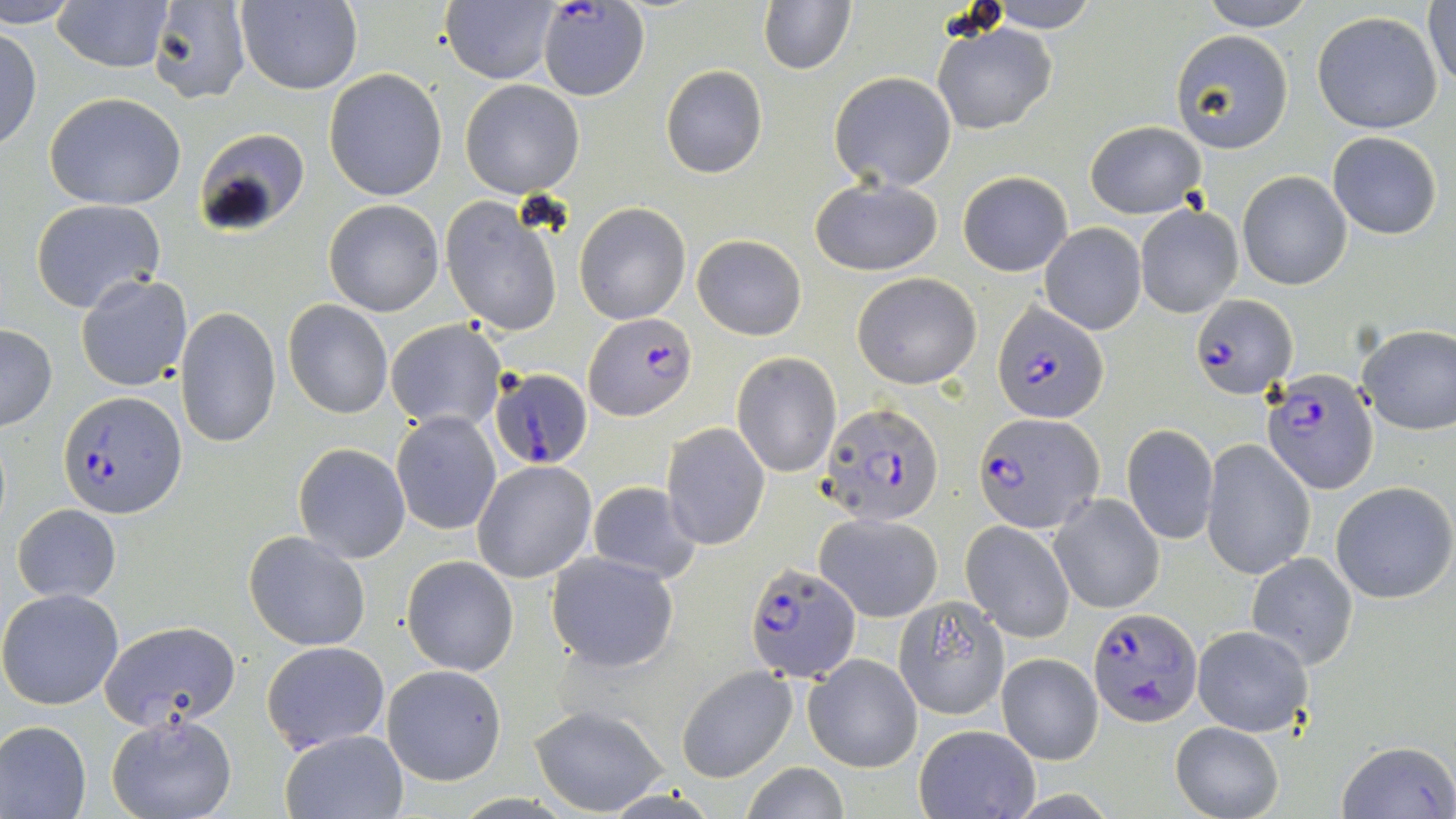 Approximate bounding boxes as named x1/y1/x2/y2 corners in pixels. Plasmodium falciparum-infected red blood cell locations (subset): (x1=1189, y1=295, x2=1296, y2=399), (x1=992, y1=300, x2=1109, y2=425), (x1=584, y1=312, x2=696, y2=420), (x1=488, y1=367, x2=594, y2=473), (x1=1262, y1=369, x2=1378, y2=495), (x1=59, y1=391, x2=187, y2=518), (x1=818, y1=403, x2=946, y2=525), (x1=973, y1=412, x2=1104, y2=534), (x1=1089, y1=606, x2=1202, y2=727). Uninfected red blood cell locations (subset): (x1=4, y1=0, x2=84, y2=28), (x1=52, y1=0, x2=175, y2=72), (x1=146, y1=0, x2=251, y2=106), (x1=440, y1=0, x2=562, y2=86), (x1=1195, y1=0, x2=1316, y2=30), (x1=234, y1=1, x2=363, y2=94), (x1=758, y1=1, x2=854, y2=74), (x1=980, y1=1, x2=1104, y2=31), (x1=1425, y1=1, x2=1456, y2=93), (x1=539, y1=3, x2=649, y2=101), (x1=1311, y1=11, x2=1444, y2=135), (x1=933, y1=23, x2=1057, y2=134), (x1=1, y1=27, x2=42, y2=152), (x1=1169, y1=30, x2=1294, y2=154), (x1=661, y1=65, x2=767, y2=178), (x1=324, y1=69, x2=447, y2=202), (x1=829, y1=72, x2=957, y2=191), (x1=459, y1=80, x2=585, y2=198), (x1=45, y1=92, x2=187, y2=210), (x1=1085, y1=120, x2=1207, y2=219), (x1=194, y1=127, x2=310, y2=234), (x1=1328, y1=131, x2=1443, y2=239), (x1=956, y1=171, x2=1072, y2=276), (x1=1238, y1=171, x2=1352, y2=290), (x1=812, y1=177, x2=945, y2=276), (x1=440, y1=198, x2=564, y2=338), (x1=31, y1=200, x2=167, y2=314), (x1=323, y1=200, x2=445, y2=317), (x1=574, y1=203, x2=691, y2=324), (x1=1135, y1=205, x2=1243, y2=318), (x1=1040, y1=222, x2=1146, y2=335), (x1=692, y1=234, x2=807, y2=340), (x1=852, y1=271, x2=982, y2=388), (x1=76, y1=274, x2=192, y2=391), (x1=282, y1=301, x2=393, y2=419), (x1=175, y1=308, x2=281, y2=448), (x1=385, y1=320, x2=506, y2=432), (x1=1358, y1=324, x2=1456, y2=434), (x1=0, y1=325, x2=56, y2=431), (x1=732, y1=352, x2=841, y2=477), (x1=391, y1=411, x2=501, y2=535), (x1=662, y1=422, x2=770, y2=550), (x1=1123, y1=423, x2=1218, y2=544), (x1=1201, y1=439, x2=1315, y2=581), (x1=293, y1=443, x2=412, y2=563), (x1=472, y1=460, x2=597, y2=582), (x1=586, y1=480, x2=701, y2=586), (x1=1330, y1=482, x2=1456, y2=604), (x1=1050, y1=493, x2=1164, y2=613), (x1=12, y1=503, x2=122, y2=603), (x1=814, y1=512, x2=944, y2=622), (x1=961, y1=521, x2=1077, y2=642), (x1=244, y1=531, x2=369, y2=651), (x1=545, y1=552, x2=679, y2=674), (x1=1247, y1=553, x2=1358, y2=670), (x1=401, y1=555, x2=520, y2=676), (x1=0, y1=588, x2=126, y2=710), (x1=893, y1=597, x2=1011, y2=719), (x1=100, y1=620, x2=242, y2=729), (x1=1192, y1=626, x2=1314, y2=737), (x1=260, y1=639, x2=389, y2=754), (x1=804, y1=652, x2=923, y2=773), (x1=995, y1=652, x2=1102, y2=764), (x1=382, y1=664, x2=506, y2=785), (x1=676, y1=666, x2=796, y2=782), (x1=530, y1=704, x2=671, y2=815), (x1=105, y1=715, x2=238, y2=819), (x1=0, y1=720, x2=93, y2=819), (x1=1170, y1=721, x2=1283, y2=819), (x1=915, y1=724, x2=1039, y2=817), (x1=281, y1=729, x2=408, y2=818), (x1=1336, y1=739, x2=1456, y2=819), (x1=741, y1=763, x2=851, y2=819). Slide-level diagnosis: Plasmodium falciparum. May-Grünwald-Giemsa-stained preparation. 1000x magnification. Image is 1456×819 pixels. Optical microscopy. Single field of view. Thin blood smear.